Classify this cell by malaria status.
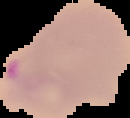
Parasitized.

image size = 130×118 pixels
preparation = thin blood smear
image type = segmented cell region with the area outside set to black